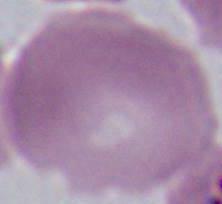

{
  "modality": "micrograph",
  "magnification": "1000x",
  "identification": "red blood cell"
}